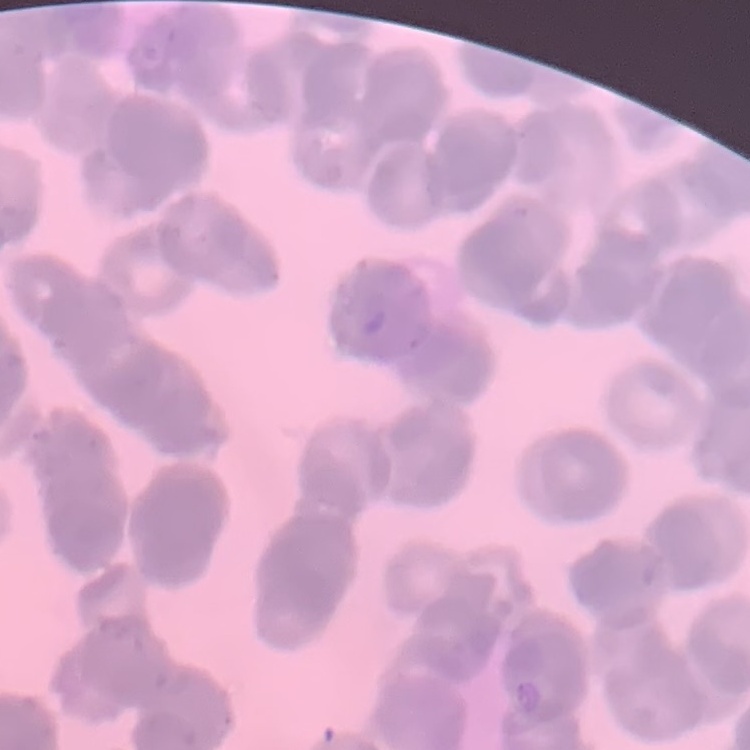

Summary:
  - Red blood cell morphology: rouleaux formation
  - Stain: Field's or Giemsa
  - Image type: one tile cut from a larger photomicrograph
  - Preparation: thin blood film